Look for Plasmodium parasites.
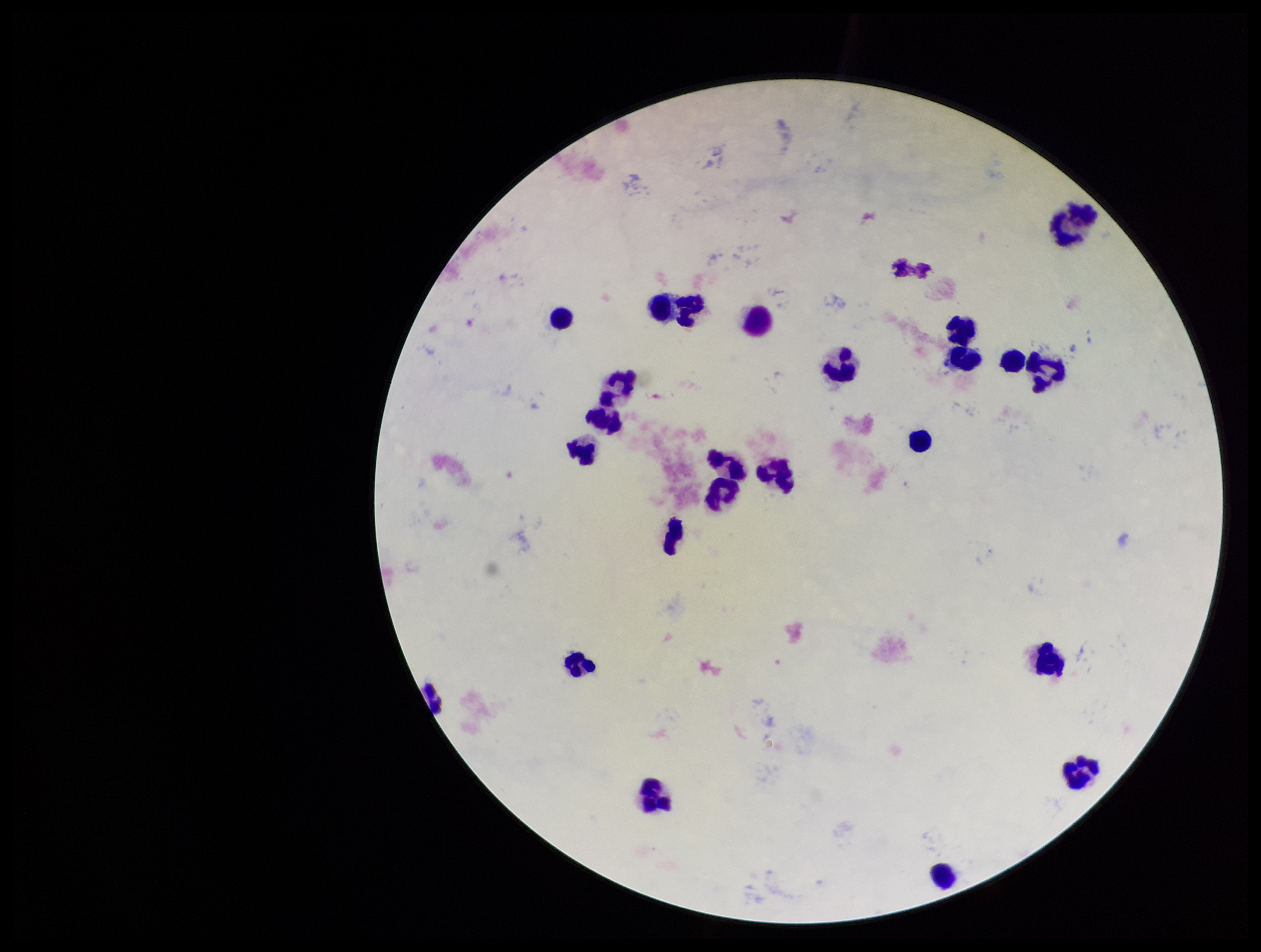
None seen.

Summary:
  - Stain: Giemsa
  - Image size: 1261×952 pixels
  - Field of view: one from this slide
  - Preparation: thick blood smear
  - Parasite count: 0
  - Leukocyte count: 24
  - Capture: smartphone photograph through the microscope eyepiece
  - Patient malaria status: negative